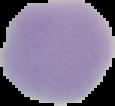
{
  "preparation": "thin blood film",
  "image_size": "115×106 pixels",
  "result": "no malaria parasites seen",
  "image_type": "segmented cell region with the area outside set to black"
}